Identify the parasite.
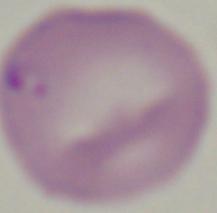
This is Babesia.

1000x magnification. Micrograph.